Identify the parasite.
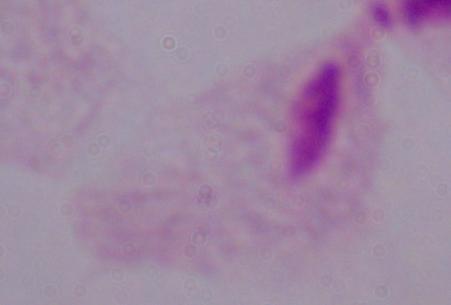
This is a trichomonad.

{
  "modality": "micrograph",
  "magnification": "1000x"
}